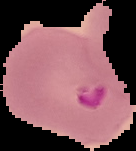
Summary:
  - Image type: segmented cell region on a black background
  - Image size: 136×151 pixels
  - Malaria status: parasitized
  - Preparation: thin blood smear